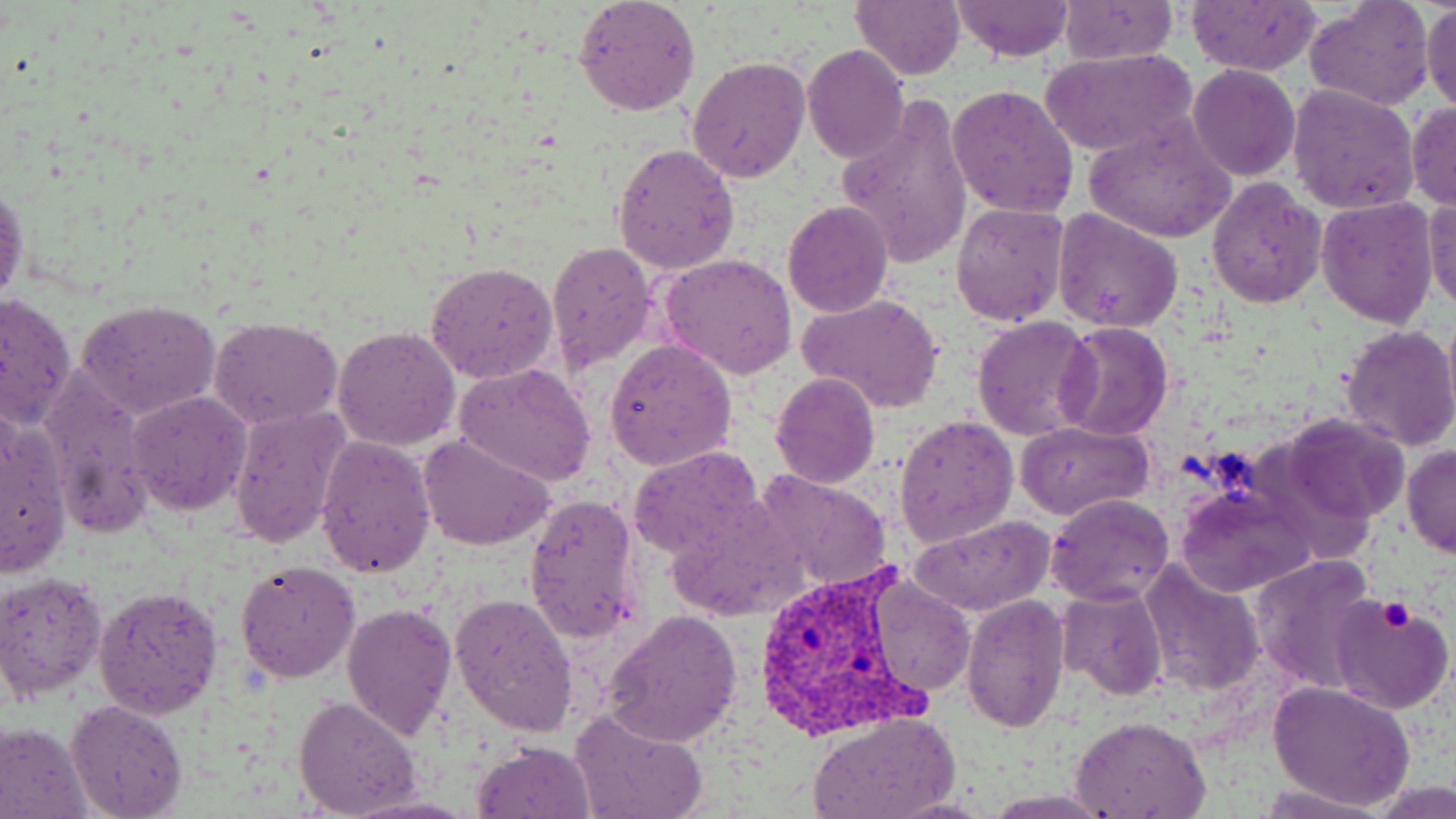

Summary:
  - Coordinate format: approximate bounding boxes as (x1, y1, x2, y2) in pixels
  - Plasmodium vivax-infected red blood cell locations: (750, 566, 927, 742)
  - Platelet locations: (1378, 600, 1414, 632)
  - Uninfected red blood cell locations: (573, 0, 702, 117), (849, 0, 963, 80), (1303, 0, 1434, 110), (951, 1, 1075, 63), (1187, 1, 1322, 74), (1422, 1, 1456, 114), (1060, 2, 1178, 66), (802, 43, 910, 164), (1042, 48, 1194, 159), (687, 56, 811, 182), (1188, 66, 1301, 182), (1288, 83, 1418, 213), (948, 84, 1079, 218), (836, 97, 973, 269), (1407, 103, 1456, 210), (1083, 118, 1237, 244), (612, 144, 740, 274), (1206, 177, 1327, 308), (0, 180, 27, 312), (1316, 195, 1438, 329), (1424, 196, 1456, 311), (782, 202, 894, 318), (950, 202, 1068, 327), (1052, 210, 1182, 333), (547, 241, 660, 370), (658, 253, 797, 378), (426, 261, 560, 386), (0, 289, 77, 429), (797, 293, 946, 414), (77, 298, 221, 418), (1442, 309, 1456, 427), (972, 315, 1096, 441), (209, 317, 342, 429), (1054, 321, 1175, 440), (1338, 323, 1456, 452), (331, 324, 461, 451), (605, 337, 737, 469), (454, 362, 597, 485), (39, 367, 155, 538), (770, 372, 880, 490), (127, 391, 252, 514), (226, 404, 350, 548), (0, 409, 72, 579), (895, 412, 1020, 548), (1281, 413, 1409, 524), (1015, 421, 1153, 520), (419, 434, 553, 552), (316, 436, 436, 578), (1401, 445, 1455, 558), (627, 446, 765, 559), (755, 469, 892, 588), (1179, 482, 1313, 596), (523, 491, 644, 644), (1046, 493, 1174, 606), (908, 516, 1054, 619), (1249, 553, 1381, 695), (237, 561, 359, 682), (1139, 562, 1263, 697), (0, 570, 106, 701), (865, 577, 975, 695), (95, 585, 224, 718), (1057, 585, 1169, 700), (449, 592, 578, 738), (961, 592, 1068, 730), (1328, 599, 1453, 716), (341, 600, 456, 741), (603, 609, 743, 746), (1269, 680, 1415, 812), (294, 697, 421, 818), (65, 700, 187, 819), (570, 706, 705, 818), (808, 709, 960, 818), (1071, 714, 1210, 817), (0, 722, 92, 818), (473, 740, 595, 818), (1258, 780, 1386, 816), (344, 794, 478, 818)
  - Slide-level diagnosis: Plasmodium vivax
  - Magnification: 1000x
  - Image size: 1456×819 pixels
  - Preparation: thin blood film
  - Modality: optical microscopy
  - Stain: May-Grünwald-Giemsa
  - Field of view: single